Identify the parasite.
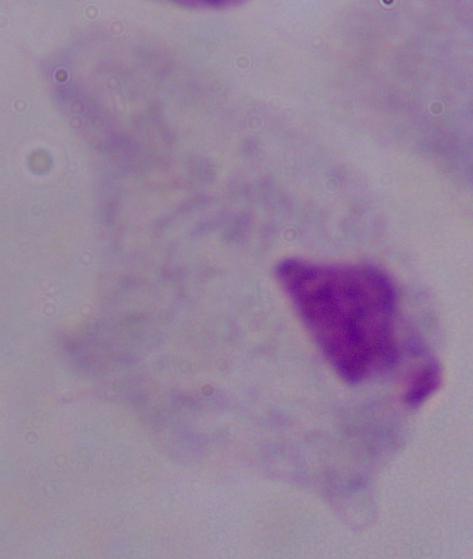

This is a trichomonad.

magnification: 1000x
modality: photomicrograph